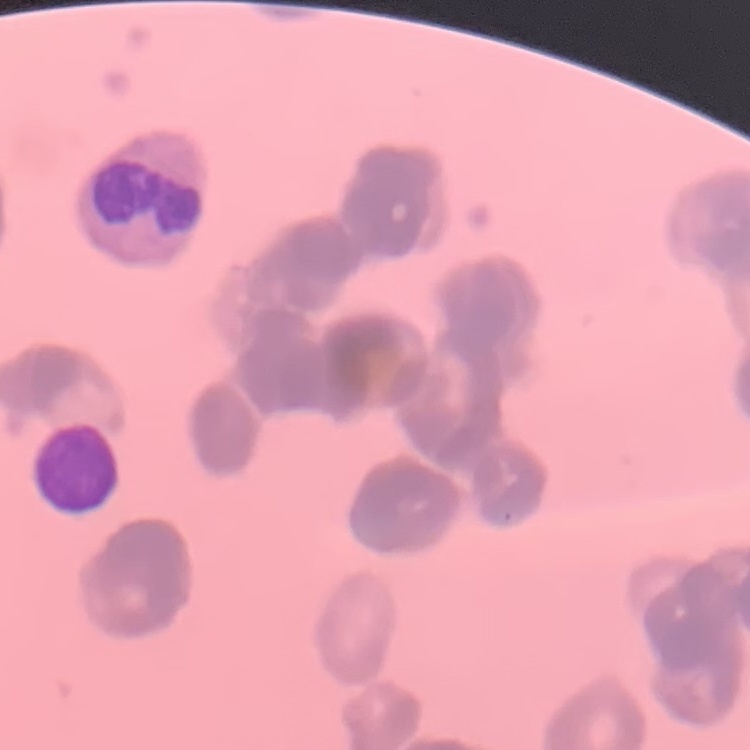
The erythrocytes exhibit rouleaux formation. Field's or Giemsa stain. One tile cut from a larger photomicrograph. Thin blood film.